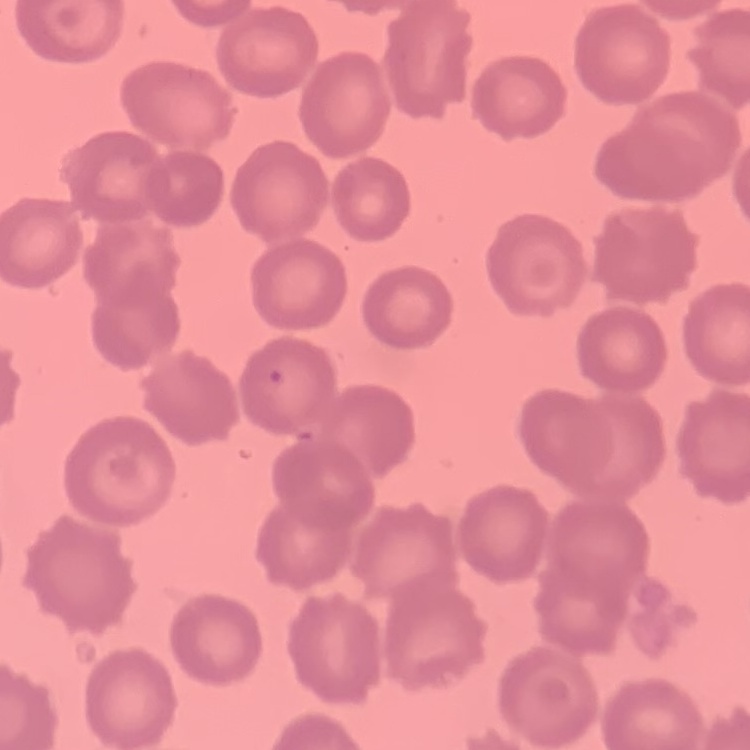

Summary:
  - Red blood cell morphology: no rouleaux formation
  - Preparation: thin blood smear
  - Stain: Field's or Giemsa
  - Image type: one tile cut from a larger photomicrograph